Describe the morphology of the red blood cells.
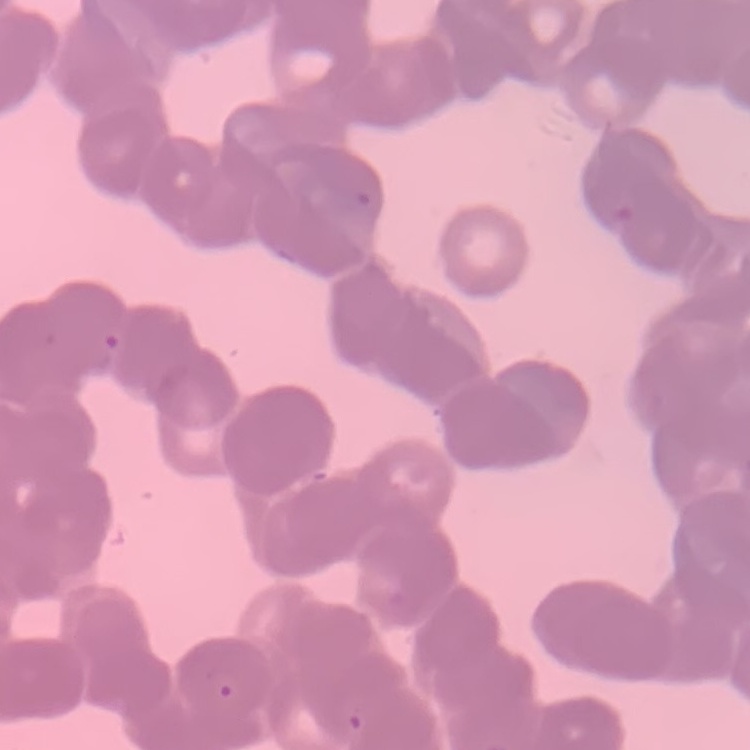
Rouleaux formation.

Thin blood smear. Stained with either Field's or Giemsa. One tile cut from a larger photomicrograph.